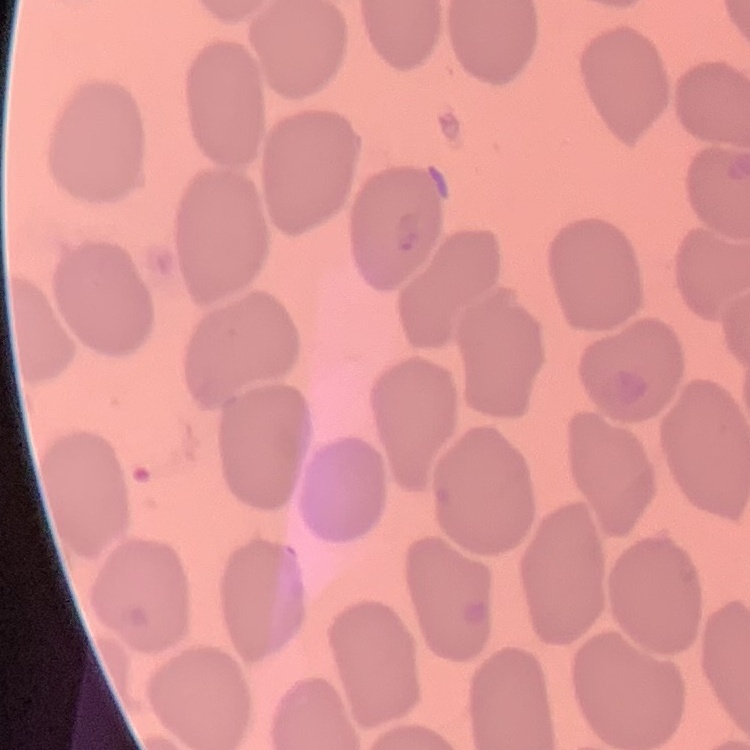 The erythrocytes show no rouleaux formation. Thin blood film. Square crop of a larger photomicrograph. Stained with either Field's or Giemsa.